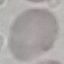

Malaria status: uninfected. Acquired by smartphone through the microscope eyepiece. Thin blood smear. Automatically extracted cell patch, resized to 64 × 64 pixels. Giemsa stain.